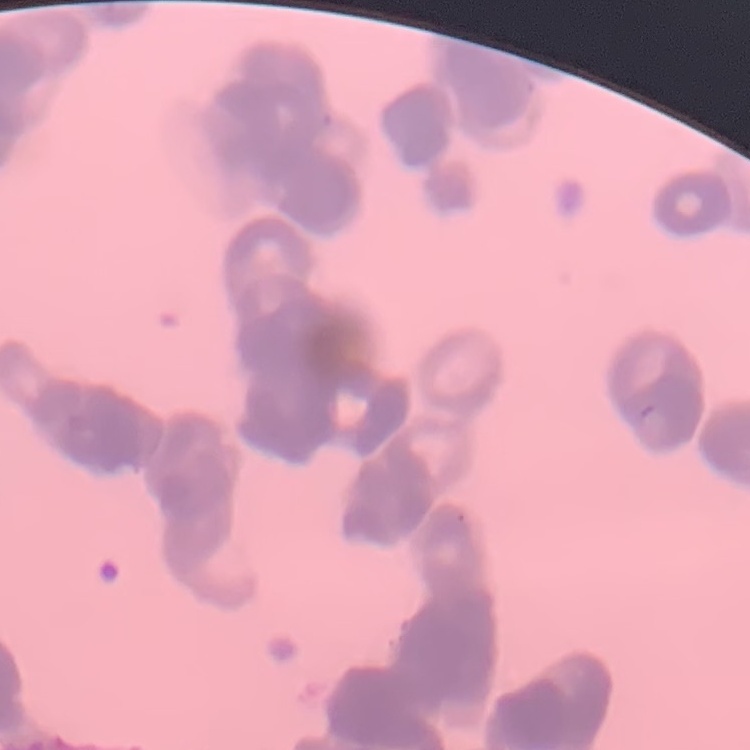

The erythrocytes show rouleaux formation. Field's or Giemsa stain. Thin blood smear. One tile cut from a larger photomicrograph.